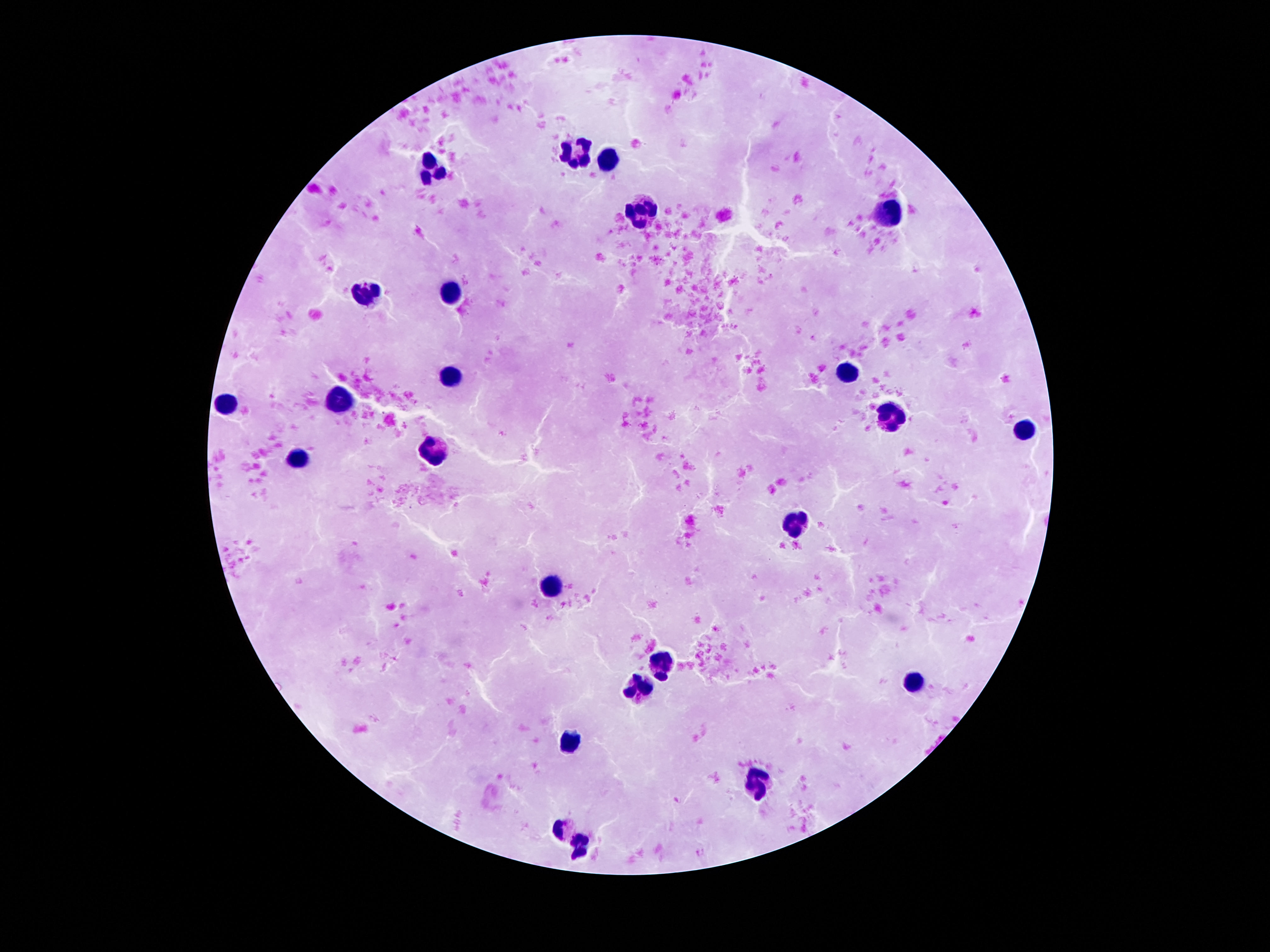 Approximate centers as [x, y] in pixels. Leukocyte locations: [577, 154], [610, 160], [432, 169], [888, 212], [642, 215], [450, 289], [364, 293], [450, 372], [847, 374], [229, 398], [337, 400], [892, 418], [1024, 430], [438, 451], [294, 455], [800, 525], [550, 587], [663, 659], [913, 681], [638, 690], [569, 740], [759, 784], [561, 831], [581, 846]. 100x magnification. One field from this slide. Giemsa stain. Thick peripheral-blood smear. Smartphone photograph taken through the microscope eyepiece. Patient malaria status: not infected. Image is 1270×952 pixels.